Name the parasite shown.
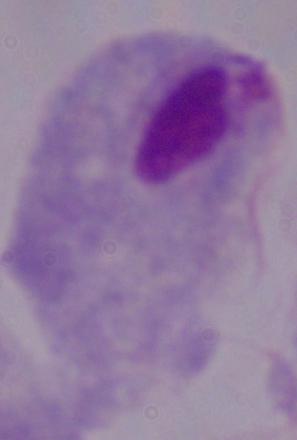

A trichomonad.

magnification = 1000x
modality = photomicrograph